Assess this cell for malaria.
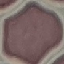

It is uninfected.

{
  "image_type": "automatically extracted cell patch, resized to 64 × 64 pixels",
  "preparation": "thin blood film",
  "stain": "Giemsa",
  "capture": "smartphone through the microscope eyepiece"
}